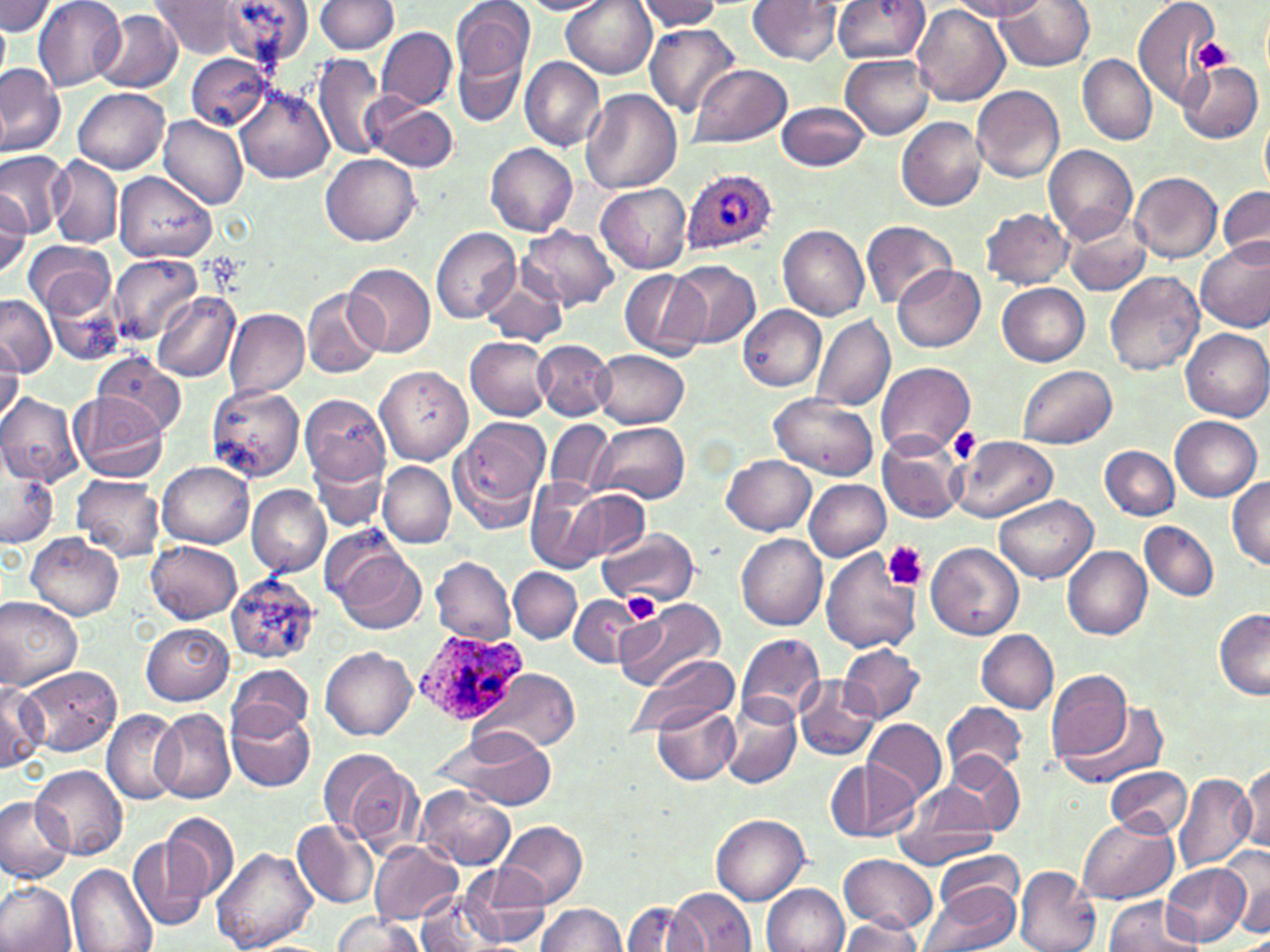

Summary:
  - Coordinate format: approximate bounding boxes as (x1, y1, x2, y2) in pixels
  - Platelet locations: (1194, 38, 1235, 73), (950, 428, 979, 463), (884, 542, 930, 591), (621, 593, 660, 624)
  - Uninfected red blood cell locations: (33, 0, 124, 91), (314, 0, 397, 54), (563, 0, 656, 78), (636, 0, 725, 31), (832, 0, 929, 63), (949, 0, 1046, 20), (1132, 0, 1225, 111), (149, 1, 245, 58), (213, 1, 312, 66), (517, 1, 611, 14), (746, 1, 843, 65), (0, 2, 59, 36), (452, 2, 533, 83), (996, 2, 1095, 73), (913, 6, 1009, 106), (94, 9, 183, 92), (0, 18, 10, 86), (643, 22, 738, 117), (451, 25, 531, 128), (377, 27, 456, 111), (313, 52, 386, 161), (185, 54, 273, 130), (840, 54, 934, 138), (1078, 54, 1156, 146), (520, 57, 606, 151), (1176, 61, 1262, 144), (689, 62, 793, 149), (0, 63, 66, 157), (233, 86, 334, 184), (972, 86, 1065, 183), (74, 87, 169, 174), (580, 89, 683, 195), (367, 100, 458, 172), (778, 101, 869, 172), (1260, 111, 1269, 196), (158, 114, 247, 211), (897, 116, 988, 212), (485, 143, 578, 236), (1044, 145, 1137, 243), (0, 149, 66, 237), (323, 153, 421, 245), (47, 155, 123, 246), (1130, 171, 1223, 263), (115, 172, 216, 262), (596, 183, 691, 272), (1218, 186, 1270, 267), (0, 190, 31, 282), (979, 207, 1074, 290), (1064, 216, 1150, 297), (862, 219, 957, 308), (519, 225, 620, 312), (778, 225, 870, 321), (430, 227, 522, 324), (1196, 238, 1270, 333), (23, 240, 115, 319), (108, 254, 202, 344), (668, 260, 761, 350), (345, 263, 436, 355), (894, 264, 985, 352), (1104, 269, 1204, 376), (619, 270, 709, 361), (479, 277, 566, 346), (44, 282, 126, 368), (998, 283, 1091, 366), (303, 288, 384, 379), (153, 293, 240, 382), (0, 295, 55, 379), (738, 305, 828, 390), (223, 308, 308, 397), (810, 313, 895, 412), (1182, 328, 1270, 421), (466, 336, 554, 420), (535, 340, 615, 419), (0, 341, 23, 426), (595, 351, 688, 428), (95, 352, 186, 434), (875, 363, 974, 458), (1019, 365, 1117, 447), (376, 366, 472, 464), (208, 385, 304, 482), (0, 391, 83, 486), (69, 392, 167, 482), (301, 393, 391, 486), (769, 394, 878, 481), (1170, 415, 1262, 500), (448, 418, 549, 532), (545, 418, 614, 498), (595, 422, 690, 504), (876, 434, 964, 524), (953, 436, 1058, 523), (309, 446, 388, 535), (1099, 446, 1180, 518), (0, 455, 59, 549), (723, 456, 817, 535), (378, 461, 456, 547), (157, 462, 254, 547), (73, 476, 165, 558), (524, 476, 610, 573), (1227, 477, 1270, 569), (804, 478, 890, 560), (247, 485, 332, 577), (563, 488, 649, 566), (994, 495, 1098, 583), (1140, 520, 1219, 600), (597, 527, 699, 606), (27, 533, 123, 620), (738, 534, 826, 630), (147, 541, 242, 623), (927, 542, 1024, 641), (820, 547, 921, 656), (1063, 547, 1152, 639), (332, 548, 427, 635), (431, 556, 515, 644), (509, 569, 582, 644), (225, 573, 319, 666), (571, 595, 646, 667), (0, 596, 83, 690), (615, 597, 727, 692), (1214, 610, 1270, 700), (142, 623, 233, 704), (977, 630, 1059, 712), (736, 633, 826, 721), (840, 643, 923, 722), (321, 647, 417, 741), (631, 656, 738, 736), (230, 663, 312, 739), (19, 666, 122, 755), (485, 668, 580, 751), (1044, 670, 1132, 764), (794, 676, 881, 760), (0, 679, 46, 772), (723, 697, 800, 789), (942, 700, 1028, 783), (1057, 700, 1171, 790), (226, 704, 315, 793), (651, 704, 737, 784), (102, 709, 185, 805), (152, 709, 237, 804), (865, 719, 946, 803), (438, 727, 558, 811), (321, 748, 421, 853), (948, 755, 1026, 835), (829, 759, 919, 841), (1239, 763, 1270, 852), (32, 764, 128, 860), (1106, 764, 1192, 839), (1173, 771, 1256, 873), (894, 783, 997, 870), (417, 787, 516, 871), (0, 796, 74, 883), (161, 813, 239, 900), (711, 814, 811, 904), (1077, 816, 1180, 903), (293, 820, 379, 910), (497, 821, 588, 908), (129, 834, 211, 932), (369, 841, 463, 925), (209, 845, 317, 952), (1225, 846, 1270, 936), (933, 849, 1024, 920), (839, 854, 937, 935), (461, 865, 551, 947), (66, 866, 157, 952), (1164, 866, 1249, 945), (1013, 867, 1101, 952), (0, 882, 76, 952), (762, 882, 848, 951), (920, 884, 1021, 952), (669, 890, 756, 951), (415, 891, 506, 952), (1104, 897, 1201, 952), (622, 900, 702, 952), (536, 902, 625, 952), (332, 912, 425, 951), (839, 918, 926, 951)
  - Plasmodium ovale-infected red blood cell locations: (681, 170, 778, 255), (414, 632, 529, 724)
  - Slide-level diagnosis: Plasmodium ovale
  - Modality: optical microscopy
  - Stain: May-Grünwald-Giemsa
  - Image size: 1270×952 pixels
  - Magnification: 1000x
  - Field of view: one of a larger specimen
  - Preparation: thin blood film